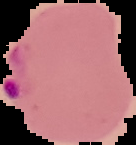
Result: malaria parasites identified. Image is 136×145 pixels. From a thin blood film. Cell region segmented out of the field of view; the surrounding area is masked to black.